State which parasite is depicted.
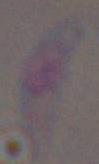
Toxoplasma gondii.

Summary:
  - Magnification: 1000x
  - Modality: micrograph